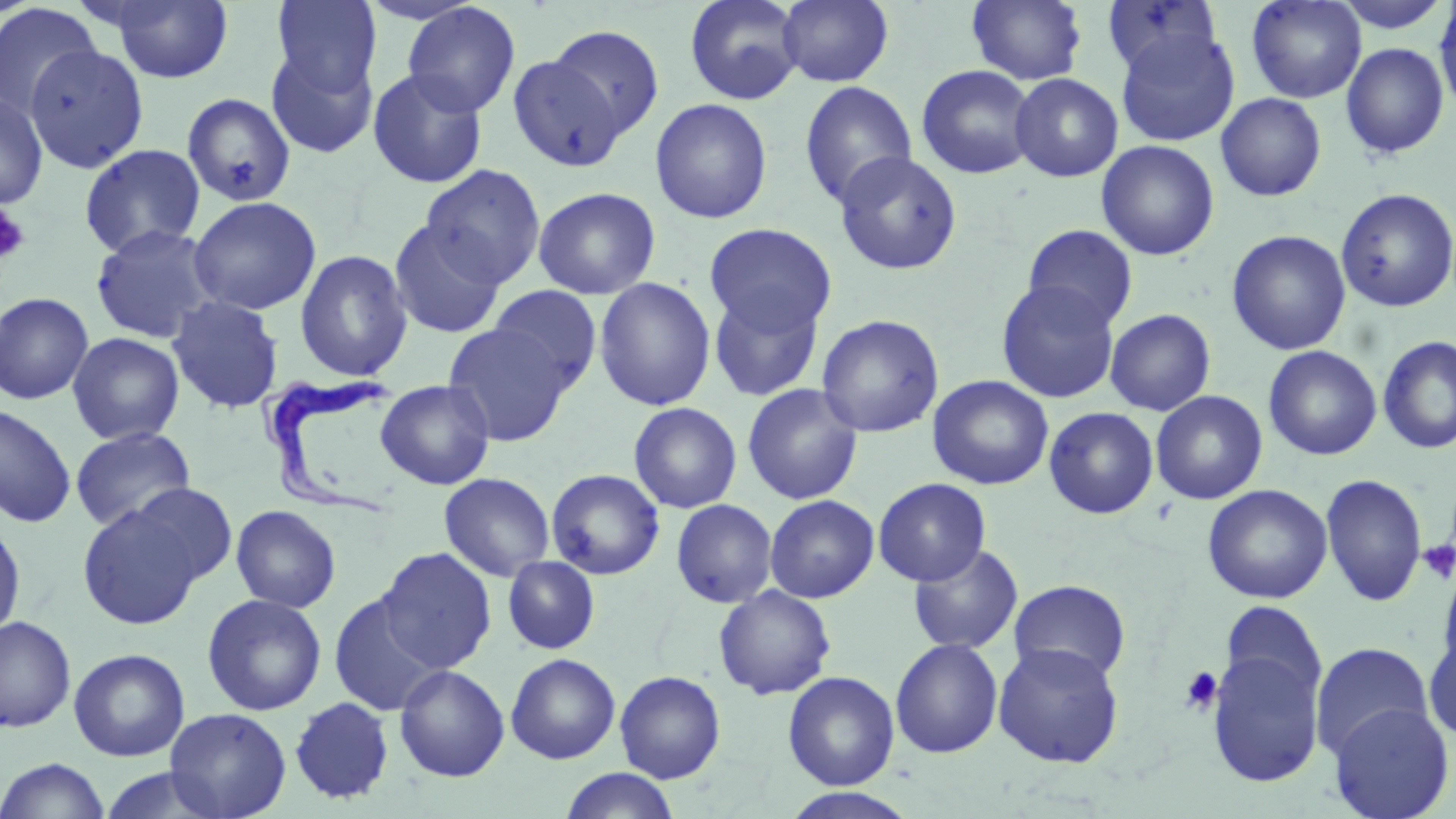

Summary:
  - Coordinate format: approximate bounding boxes as [x1, y1, x2, y2] in pixels
  - Uninfected red blood cell locations: [271, 0, 382, 97], [684, 0, 805, 105], [777, 0, 894, 87], [1101, 0, 1222, 79], [1246, 0, 1366, 104], [1332, 0, 1452, 34], [100, 1, 235, 83], [966, 1, 1088, 85], [401, 2, 521, 117], [1434, 2, 1456, 116], [0, 3, 102, 122], [545, 24, 665, 141], [1114, 28, 1241, 147], [23, 42, 149, 174], [1340, 42, 1450, 159], [265, 47, 378, 159], [508, 53, 626, 171], [916, 64, 1038, 179], [367, 68, 488, 189], [1010, 73, 1124, 182], [799, 80, 918, 208], [0, 92, 49, 210], [181, 92, 298, 207], [1215, 93, 1327, 202], [649, 98, 773, 224], [1096, 140, 1219, 261], [79, 143, 205, 258], [833, 150, 963, 276], [421, 165, 546, 288], [532, 187, 660, 300], [1336, 188, 1456, 313], [188, 196, 322, 316], [389, 219, 506, 339], [703, 222, 837, 336], [89, 224, 221, 344], [1022, 224, 1138, 330], [1226, 229, 1351, 356], [294, 249, 413, 382], [593, 277, 716, 412], [995, 279, 1121, 403], [488, 285, 603, 392], [708, 289, 825, 402], [0, 291, 94, 405], [166, 295, 285, 414], [1105, 308, 1216, 416], [816, 314, 944, 438], [443, 323, 574, 446], [67, 332, 185, 445], [1378, 334, 1456, 455], [1263, 344, 1382, 460], [927, 375, 1054, 490], [374, 379, 495, 490], [741, 383, 864, 505], [1150, 390, 1268, 505], [628, 402, 742, 514], [0, 403, 77, 528], [1044, 406, 1159, 519], [70, 426, 196, 532], [546, 468, 665, 580], [438, 472, 555, 582], [1320, 473, 1428, 607], [872, 477, 991, 586], [130, 483, 238, 585], [1202, 483, 1333, 604], [765, 494, 879, 603], [671, 498, 778, 608], [77, 503, 202, 630], [230, 505, 341, 613], [0, 519, 26, 642], [907, 543, 1023, 654], [376, 547, 497, 673], [503, 556, 600, 655], [1435, 562, 1456, 683], [1008, 579, 1131, 684], [713, 585, 837, 700], [328, 592, 444, 716], [202, 593, 327, 716], [1220, 601, 1327, 708], [0, 616, 76, 733], [0, 622, 149, 751], [1423, 630, 1456, 743], [889, 638, 1004, 759], [992, 642, 1125, 767], [1206, 642, 1325, 789], [1310, 642, 1434, 762], [69, 648, 190, 761], [505, 653, 620, 764], [394, 664, 509, 782], [614, 670, 725, 783], [782, 670, 900, 790], [289, 696, 395, 805], [1328, 702, 1454, 819], [164, 707, 292, 819], [0, 757, 110, 819], [560, 768, 680, 819], [783, 787, 916, 819]
  - Platelet locations: [0, 202, 31, 266], [1418, 539, 1456, 584], [1180, 666, 1223, 715]
  - Trypanosoma brucei locations: [259, 373, 405, 523]
  - Slide-level diagnosis: Trypanosoma brucei
  - Stain: May-Grünwald-Giemsa
  - Magnification: 1000x
  - Image size: 1456×819 pixels
  - Field of view: one of a larger specimen
  - Modality: light microscopy
  - Preparation: thin blood smear